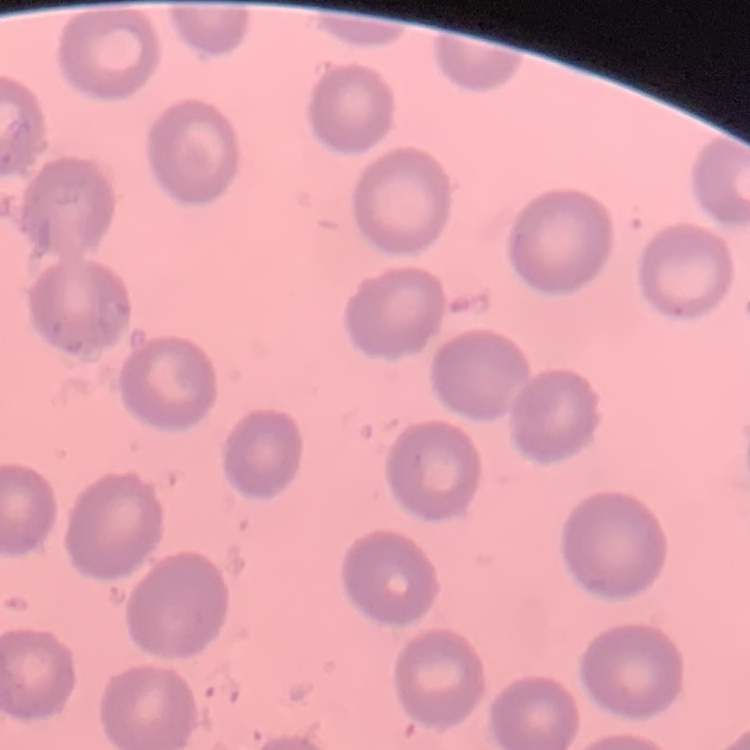 The erythrocytes show no rouleaux formation. Field's or Giemsa stain. Thin blood film. Square crop of a larger photomicrograph.